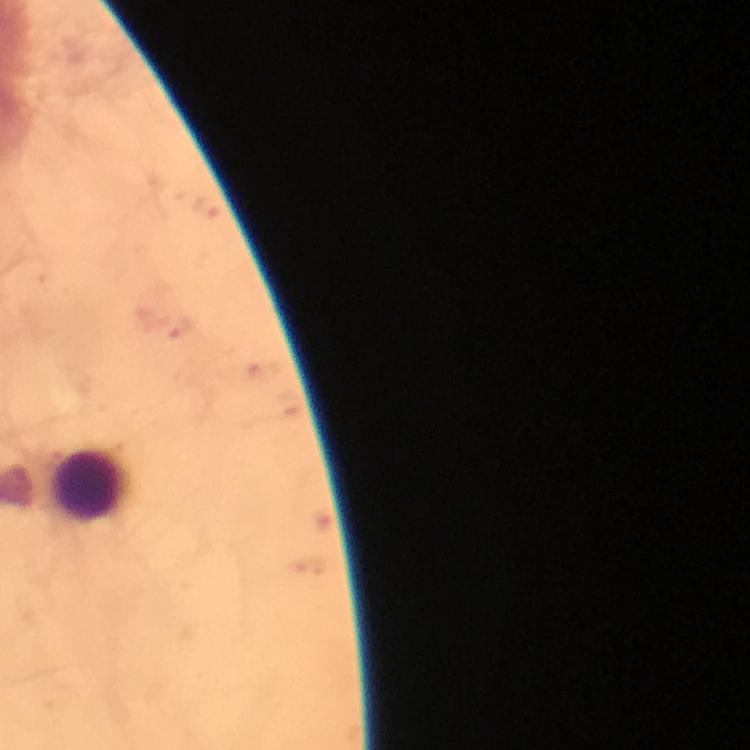

{
  "stain": "Giemsa",
  "plasmodium_parasites": "none seen",
  "magnification": "100x",
  "immersion_oil": "applied",
  "capture": "smartphone camera through the microscope",
  "image_size": "750×750 pixels",
  "cropped_from": "a single field of view",
  "context": "from a malaria diagnostic workup",
  "leukocyte_locations": "approximate object centers, in pixels from the top-left corner: (x=91, y=487)",
  "preparation": "thick blood film"
}